Assess this cell for malaria.
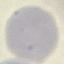

It is uninfected.

Summary:
  - Image type: cell patch, automatically extracted from a larger field of view and resized to 64 × 64 pixels
  - Capture: smartphone through the microscope eyepiece
  - Preparation: thin blood smear
  - Stain: Giemsa